Evaluate for malaria.
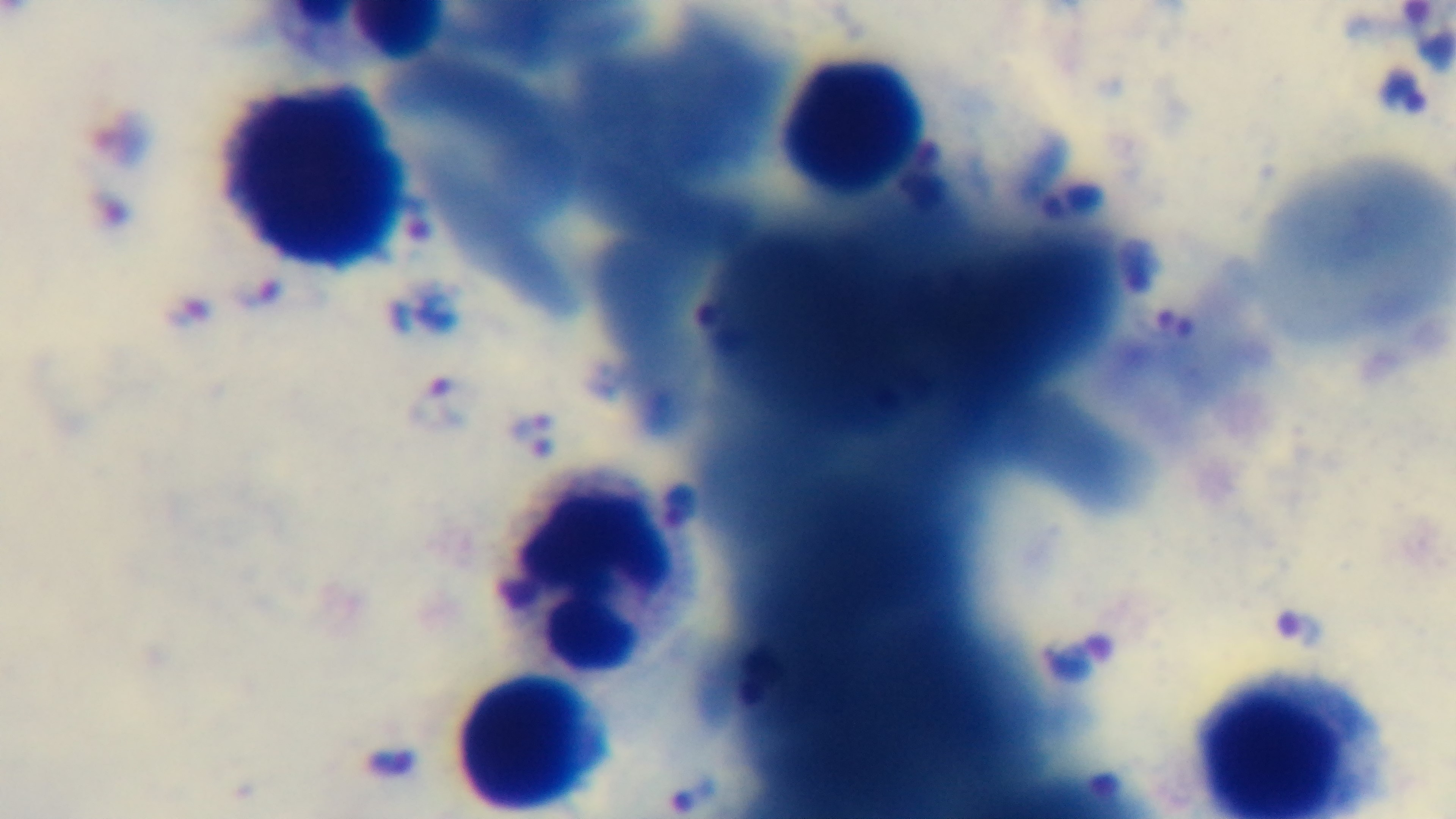

Infected.

{
  "modality": "light microscopy",
  "capture": "mounted 4K digital camera",
  "preparation": "thick blood film",
  "objective": "100x oil immersion",
  "field_of_view": "one from the slide",
  "stain": "Giemsa"
}